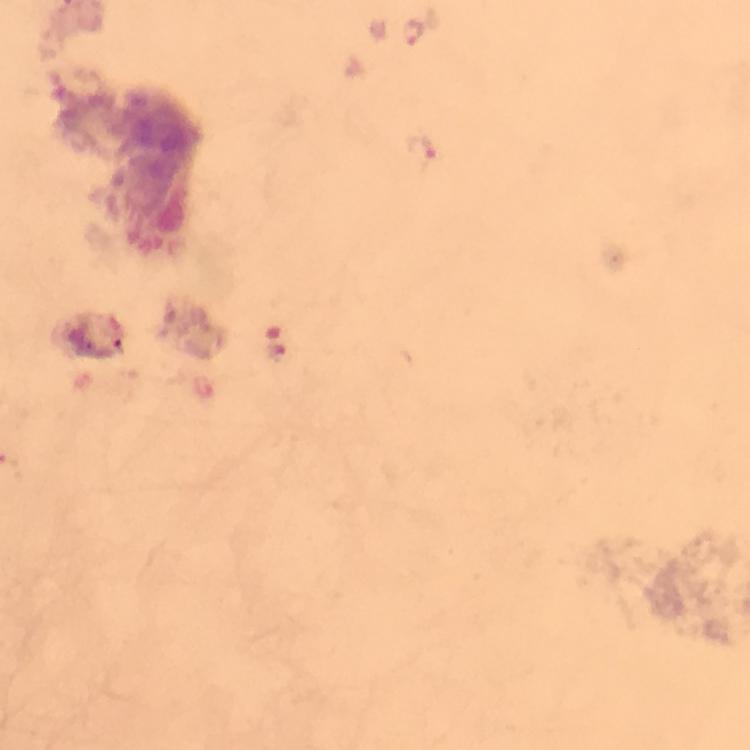
Approximate centers as [x, y] in pixels. Plasmodium parasite locations: [413, 30], [421, 149], [278, 350]. Image is 750×750 pixels. Giemsa stain. At 100x magnification. Thick blood smear. Photographed with a smartphone mounted on the microscope. Immersion oil applied. From a malaria diagnostic workup. Cropped region of a single field of view.